Classify this cell by malaria status.
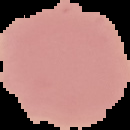
It is uninfected.

preparation = thin blood film
image type = segmented cell region with the area outside set to black
image size = 130×130 pixels